Identify the parasite.
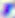
This is Toxoplasma gondii.

Summary:
  - Magnification: 400x
  - Modality: photomicrograph